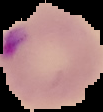
result = Plasmodium parasites detected
preparation = thin blood smear
image size = 103×112 pixels
image type = cell region segmented out of the field of view; surrounding area masked to black